Locate every Plasmodium parasite and every leukocyte.
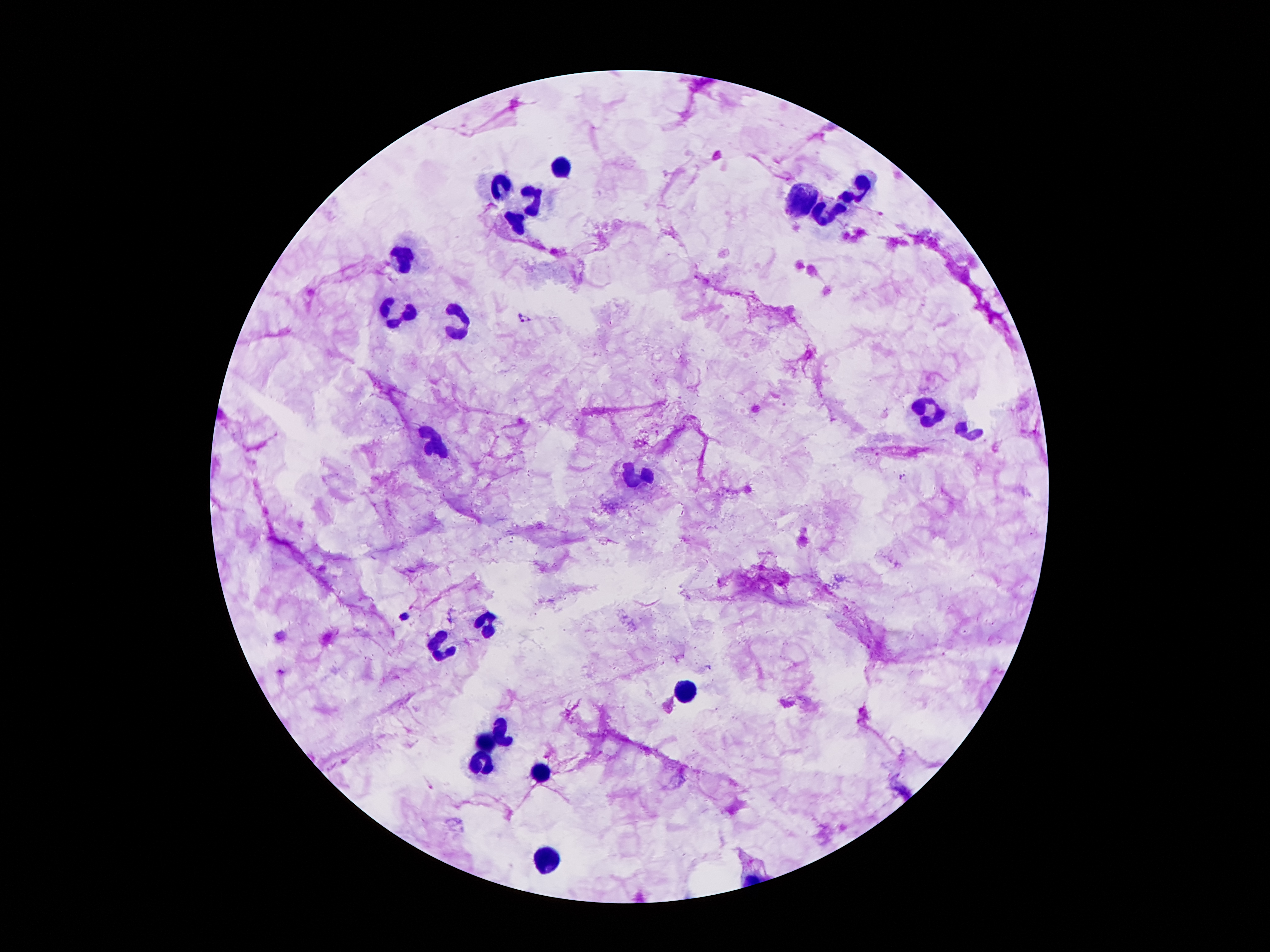

Approximate object centers, in pixels from the top-left corner.
Plasmodium parasites: (x=526, y=318), (x=901, y=476).
Leukocytes: (x=560, y=171), (x=501, y=186), (x=857, y=188), (x=533, y=198), (x=805, y=201), (x=832, y=211), (x=515, y=225), (x=406, y=257), (x=397, y=312), (x=459, y=323), (x=927, y=414), (x=968, y=433), (x=442, y=445), (x=635, y=477), (x=486, y=626), (x=439, y=650), (x=685, y=692), (x=502, y=729), (x=486, y=741), (x=481, y=762), (x=541, y=770), (x=551, y=861).

Summary:
  - Magnification: 100x
  - Image size: 1270×952 pixels
  - Preparation: thick blood smear
  - Stain: Giemsa
  - Field of view: single
  - Patient malaria status: positive for Plasmodium falciparum
  - Capture: smartphone through the microscope eyepiece